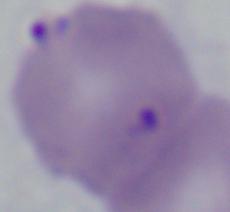
Summary:
  - Identification: Babesia
  - Modality: photomicrograph
  - Magnification: 1000x